Locate and identify every blood parasite.
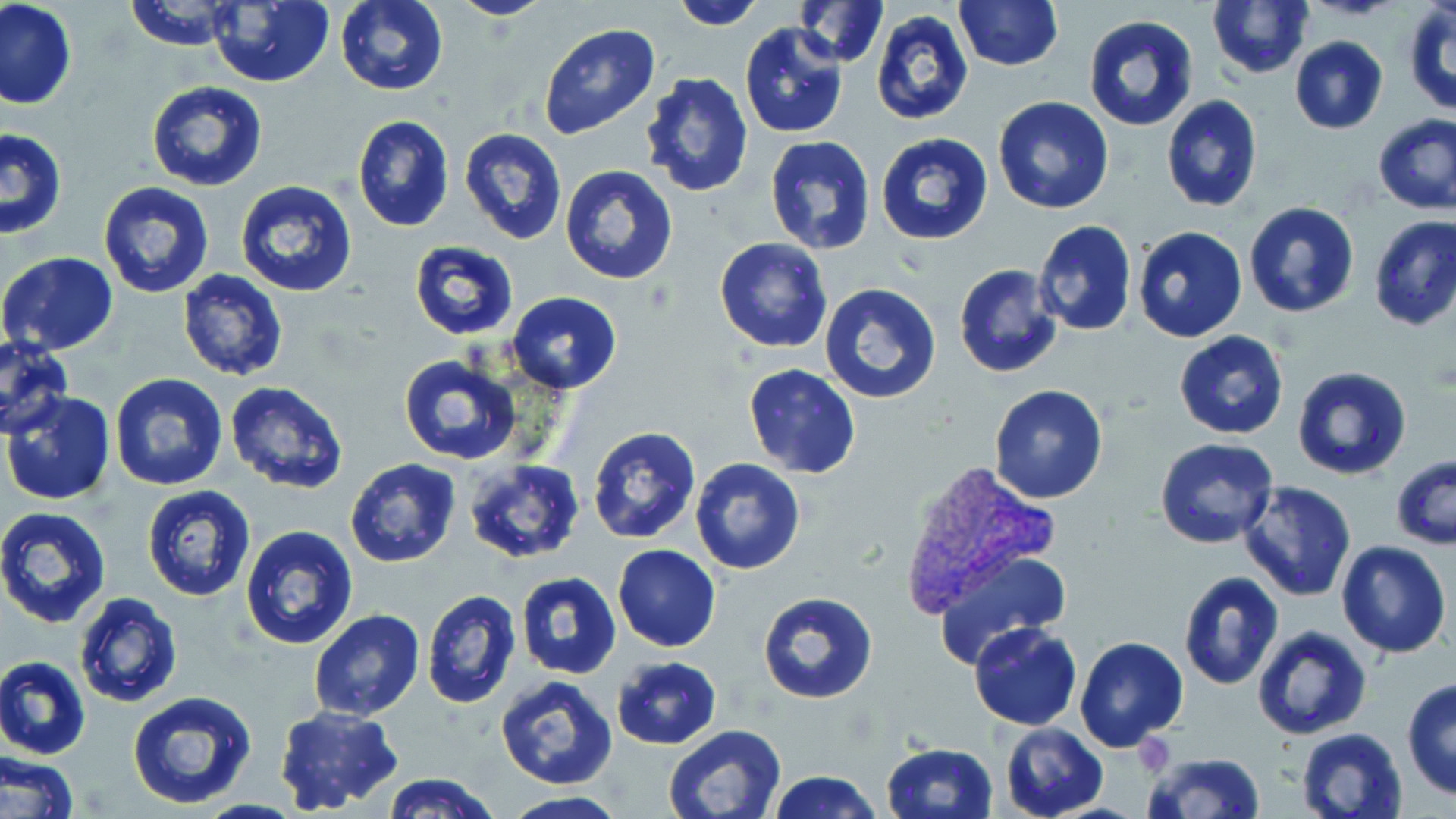
Approximate bounding boxes as (x1, y1, x2, y2) in pixels.
Plasmodium vivax-infected red blood cells: (897, 459, 1061, 619).
No Plasmodium falciparum, Plasmodium ovale, Plasmodium malariae, Babesia divergens, or Trypanosoma brucei observed.

slide_level_diagnosis: Plasmodium vivax
uninfected_red_blood_cell_locations: 'approximate bounding boxes as (x1, y1, x2, y2) in pixels: (125, 0, 241, 50), (336, 0, 449, 96), (449, 0, 556, 22), (667, 0, 767, 29), (793, 0, 888, 67), (953, 0, 1065, 72), (1, 1, 77, 110), (207, 1, 335, 87), (1206, 1, 1314, 80), (1403, 3, 1456, 116), (870, 10, 974, 126), (1081, 16, 1199, 133), (738, 22, 848, 138), (538, 23, 660, 139), (1289, 36, 1388, 135), (640, 71, 754, 197), (146, 80, 267, 193), (1160, 95, 1263, 214), (990, 96, 1115, 216), (1372, 113, 1456, 215), (352, 114, 455, 233), (0, 126, 68, 240), (458, 127, 568, 246), (875, 132, 994, 245), (765, 135, 876, 255), (559, 164, 678, 285), (98, 180, 214, 298), (234, 180, 359, 299), (1244, 201, 1359, 318), (1368, 215, 1456, 332), (1032, 220, 1138, 337), (1131, 226, 1249, 344), (714, 239, 832, 352), (408, 240, 519, 340), (1, 250, 120, 355), (953, 264, 1066, 381), (176, 269, 288, 382), (820, 281, 941, 403), (505, 291, 624, 395), (1174, 331, 1289, 440), (0, 336, 74, 439), (399, 354, 524, 464), (742, 364, 862, 480), (1291, 366, 1413, 481), (110, 374, 229, 491), (223, 381, 348, 496), (988, 383, 1108, 504), (3, 391, 118, 509), (587, 426, 702, 545), (1154, 438, 1278, 550), (1186, 452, 1320, 581), (461, 455, 586, 566), (1391, 456, 1455, 551), (689, 458, 806, 575), (345, 459, 461, 568), (1239, 481, 1358, 603), (141, 486, 256, 602), (0, 506, 113, 628), (240, 524, 360, 648), (1336, 539, 1451, 658), (612, 544, 721, 651), (933, 549, 1071, 666), (514, 572, 622, 679), (1177, 572, 1286, 692), (421, 591, 520, 708), (758, 591, 877, 704), (74, 592, 184, 709), (309, 608, 424, 721), (969, 622, 1082, 731), (1252, 625, 1371, 740), (1075, 635, 1189, 754), (0, 656, 92, 759), (611, 656, 722, 750), (495, 673, 619, 790), (1402, 678, 1456, 801), (127, 691, 257, 811), (275, 706, 403, 815), (999, 721, 1109, 819), (660, 724, 786, 819), (1296, 727, 1408, 819), (883, 742, 999, 819), (0, 749, 80, 819), (1143, 752, 1267, 819), (767, 771, 883, 819), (381, 772, 497, 819), (500, 793, 628, 818)'
modality: light microscopy
stain: May-Grünwald-Giemsa
field_of_view: single
magnification: 1000x
image_size: 1456×819 pixels
preparation: thin blood film